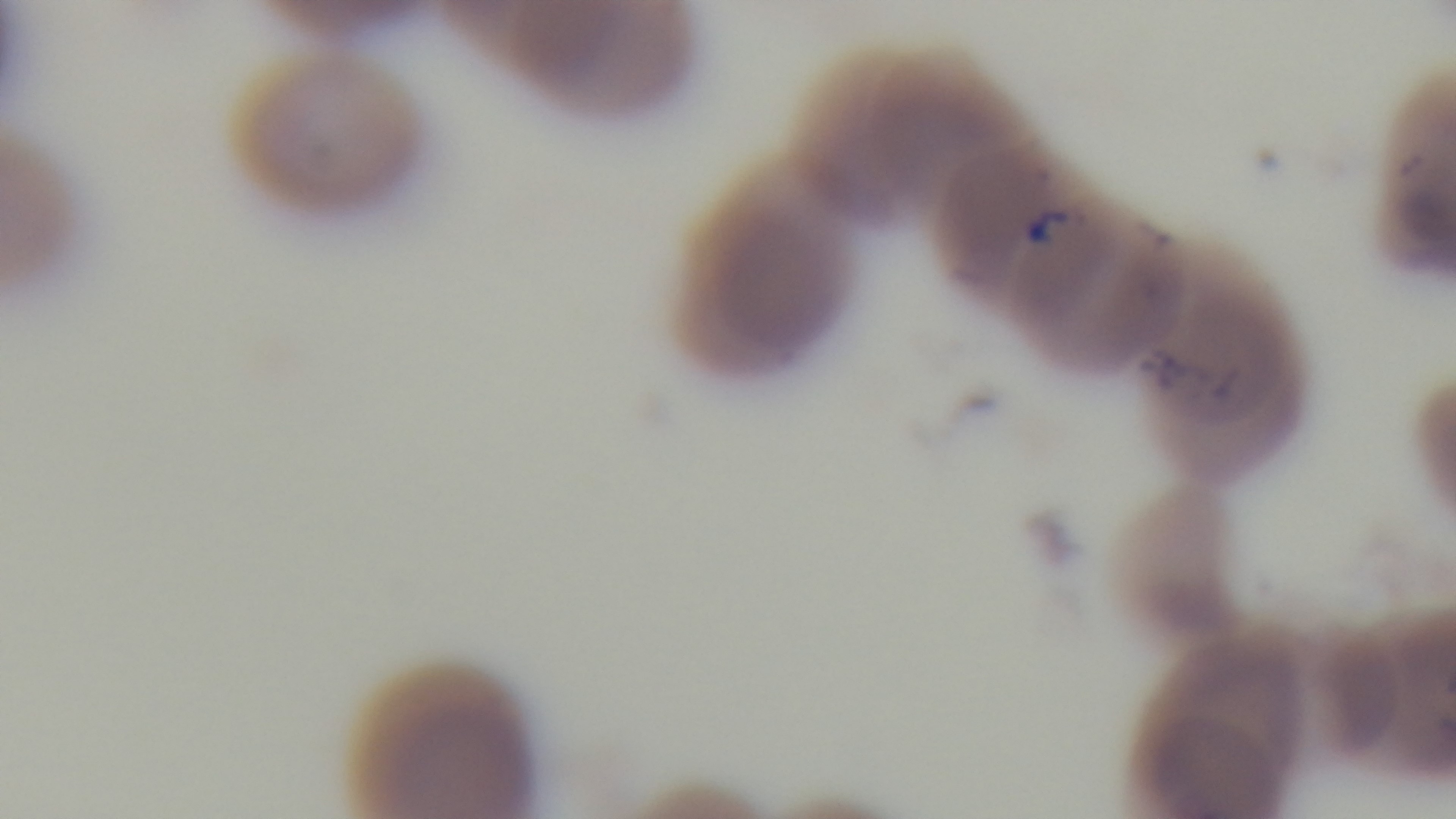
{
  "modality": "light microscopy",
  "preparation": "thin blood film",
  "objective": "100x oil immersion",
  "field_of_view": "single",
  "stain": "Giemsa",
  "capture": "mounted 4K digital camera",
  "malaria_status": "positive"
}